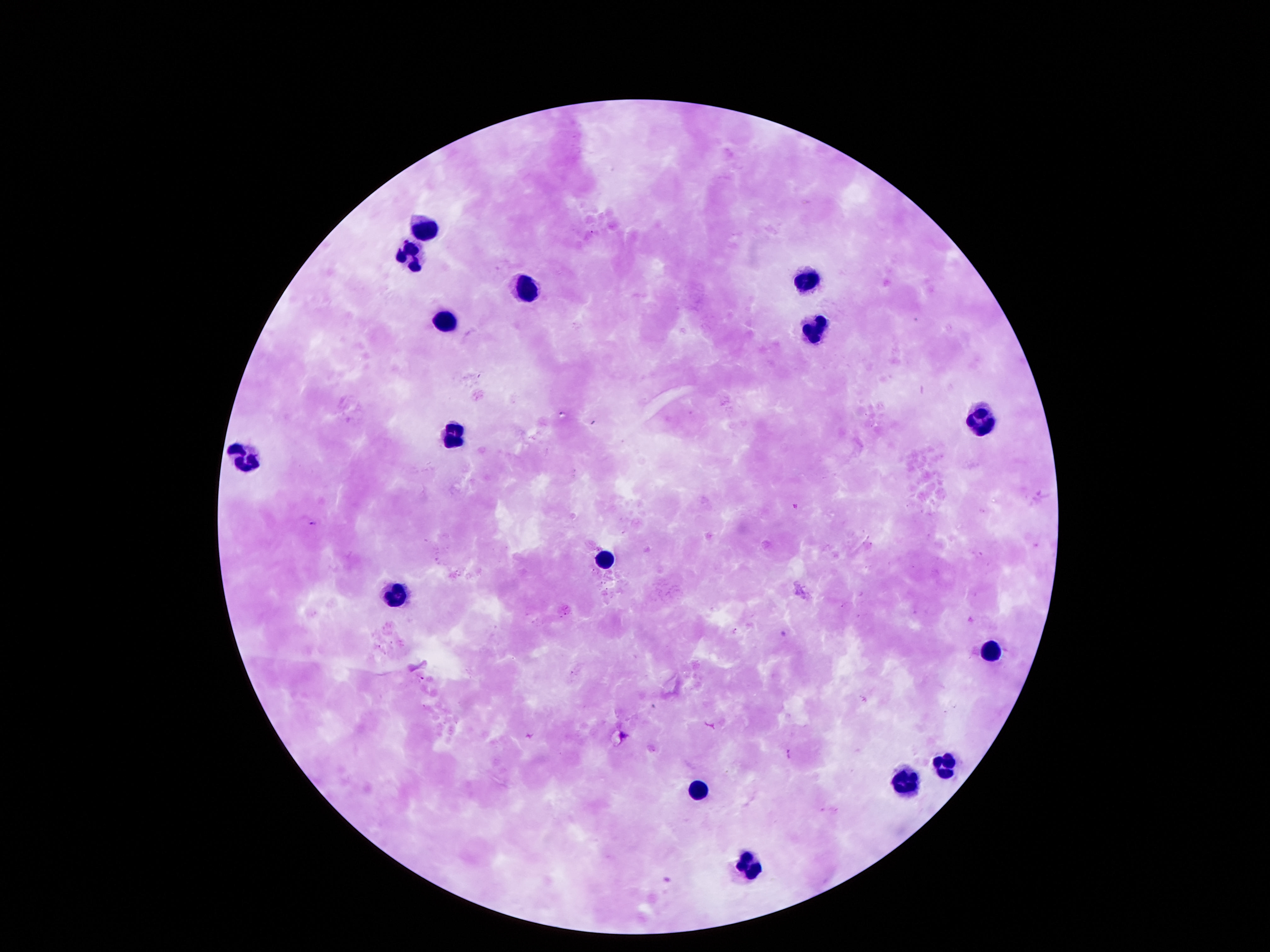 Approximate object centers, in pixels from the top-left corner. Leukocyte locations: (x=427, y=225), (x=406, y=257), (x=807, y=279), (x=518, y=293), (x=446, y=326), (x=813, y=329), (x=981, y=416), (x=449, y=434), (x=244, y=456), (x=605, y=558), (x=393, y=593), (x=988, y=649), (x=941, y=766), (x=904, y=783), (x=698, y=794), (x=745, y=870). 100x magnification. Image is 1270×952 pixels. Giemsa stain. Thick peripheral-blood smear. Photographed through the microscope eyepiece with a smartphone camera. Patient malaria status: uninfected. One field from this slide.